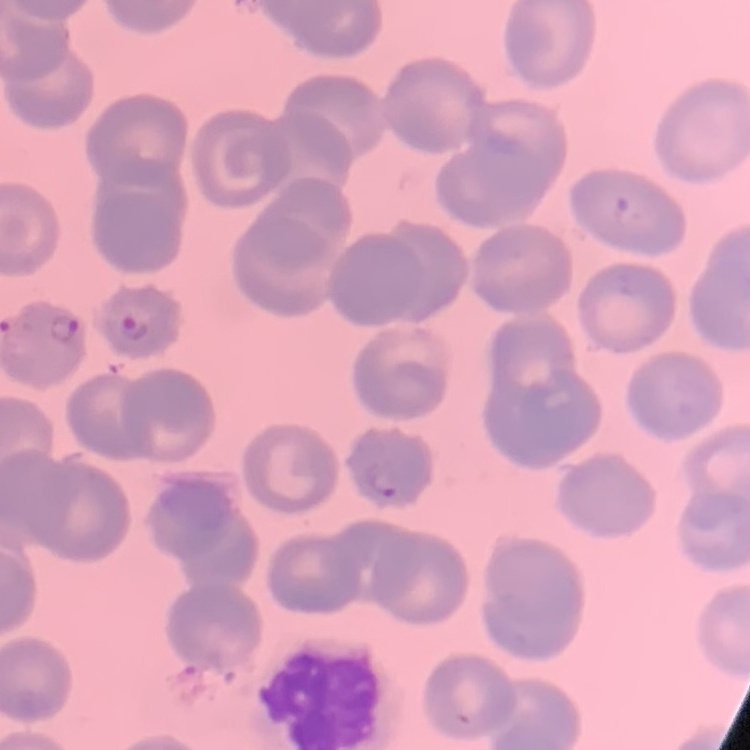

The red blood cells exhibit no rouleaux formation. Thin peripheral smear. One tile cut from a larger photomicrograph. Field's or Giemsa stain.